Identify the preparation type.
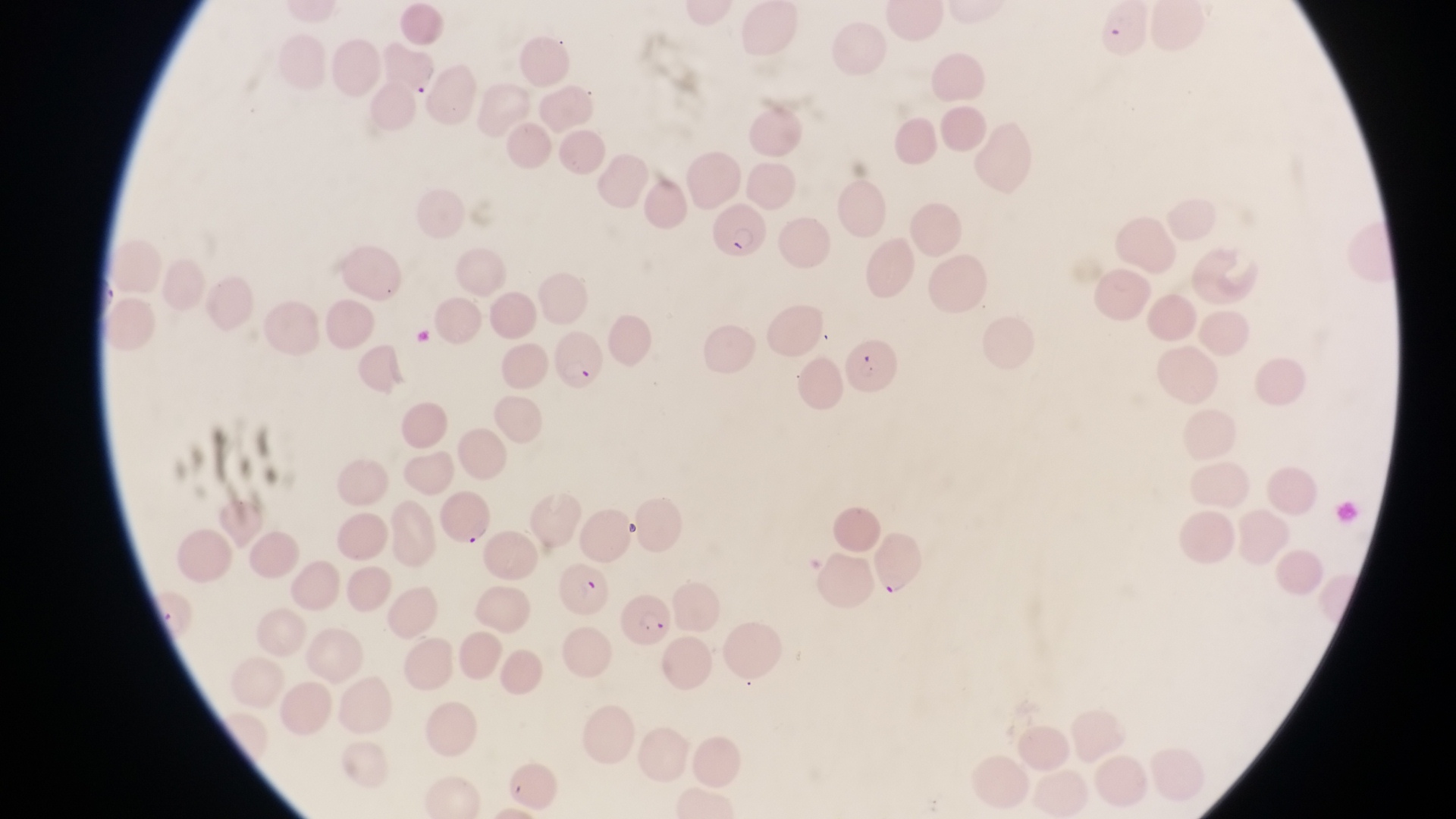

Thin blood film.

Approximate bounding boxes as left top right bottom in pixels.
Summary:
  - Parasitised red blood cell locations: 711 201 767 257; 548 325 607 396; 842 337 901 398; 441 491 496 546; 874 534 927 592; 555 566 619 619; 623 589 682 656
  - Magnification: 1000x
  - Image size: 1456×819 pixels
  - Field of view: single
  - Capture: smartphone photograph through the eyepiece of an Olympus CX-23 microscope
  - Country: Uganda